Assess this cell for malaria.
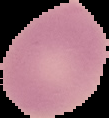
It is uninfected.

Summary:
  - Preparation: thin blood film
  - Image type: segmented cell region with the area outside set to black
  - Image size: 109×118 pixels